Give the extent of all Plasmodium ovale-infected red blood cells.
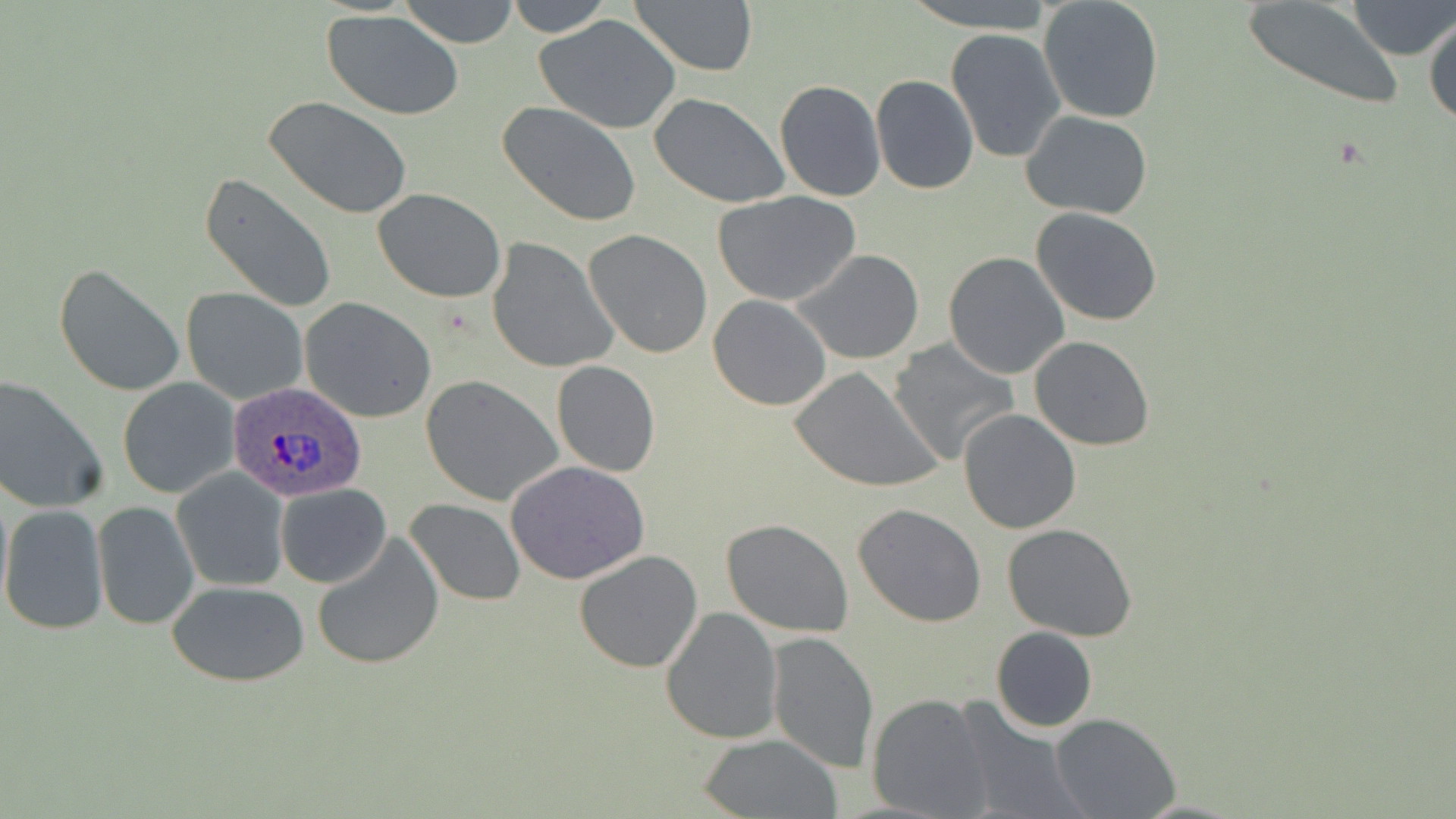

Approximate bounding boxes as (x1,y1)-(x2,y2) corner pairs in pixels.
Plasmodium ovale-infected red blood cells: (228,382)-(366,502).

{
  "slide_level_diagnosis": "Plasmodium ovale",
  "magnification": "1000x",
  "stain": "May-Grünwald-Giemsa",
  "image_size": "1456×819 pixels",
  "field_of_view": "single",
  "modality": "light microscopy",
  "uninfected_red_blood_cell_locations": "approximate bounding boxes as (x1,y1)-(x2,y2) corner pairs in pixels: (399,0)-(520,48), (505,0)-(613,36), (628,0)-(760,78), (903,0)-(1056,32), (1237,0)-(1408,112), (1349,0)-(1454,60), (1038,1)-(1165,122), (322,9)-(466,120), (1424,10)-(1455,129), (535,15)-(682,134), (948,16)-(1161,143), (945,29)-(1065,163), (871,75)-(978,194), (773,80)-(886,202), (648,93)-(791,207), (264,96)-(414,222), (498,102)-(642,227), (1020,110)-(1153,220), (200,171)-(338,315), (373,189)-(506,303), (715,192)-(861,307), (1030,207)-(1163,328), (583,229)-(713,360), (487,238)-(618,374), (793,248)-(925,364), (942,252)-(1070,378), (54,262)-(186,398), (181,287)-(307,405), (706,294)-(832,410), (301,298)-(438,424), (1028,336)-(1154,451), (888,339)-(1022,467), (550,360)-(661,476), (789,367)-(943,493), (0,374)-(107,514), (420,377)-(563,506), (118,378)-(238,499), (957,408)-(1083,534), (506,459)-(651,586), (172,468)-(290,592), (0,477)-(12,615), (276,482)-(392,588), (405,499)-(525,604), (91,501)-(200,631), (852,504)-(987,626), (0,505)-(108,636), (721,519)-(852,638), (1003,524)-(1137,643), (311,529)-(445,670), (574,550)-(703,673), (168,581)-(310,685), (661,607)-(782,743), (989,626)-(1098,732), (766,631)-(879,772), (867,692)-(995,817), (952,696)-(1090,819), (1050,712)-(1180,819), (698,732)-(842,818)",
  "preparation": "thin blood film"
}